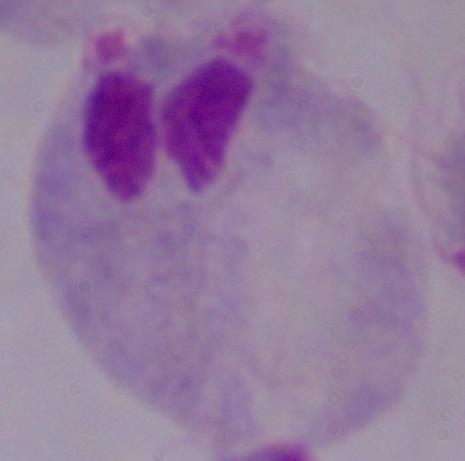
modality = micrograph
identification = trichomonad
magnification = 1000x